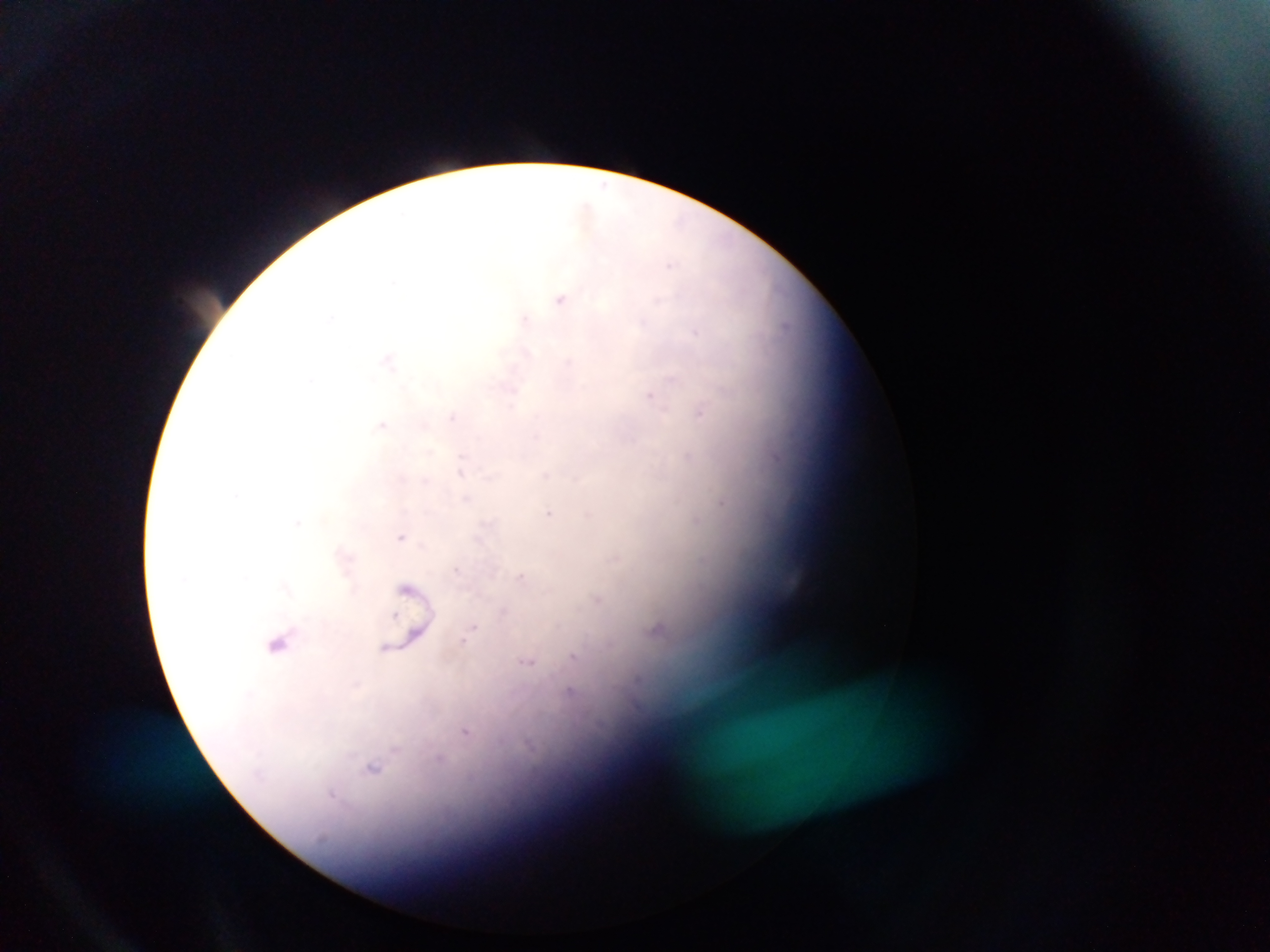
Approximate centers as {x, y} in pixels.
Summary:
  - Malaria parasite locations: {562, 298}, {527, 320}, {389, 361}, {652, 396}, {702, 413}, {454, 417}, {384, 424}, {688, 456}, {551, 513}, {696, 519}, {402, 536}, {522, 576}, {598, 600}, {657, 629}, {470, 631}, {278, 643}, {575, 655}, {527, 662}, {571, 691}, {466, 731}, {372, 768}
  - Country: Ghana
  - Capture: mobile-phone photograph through a microscope
  - Preparation: thick blood film
  - Field of view: single
  - Image size: 1270×952 pixels